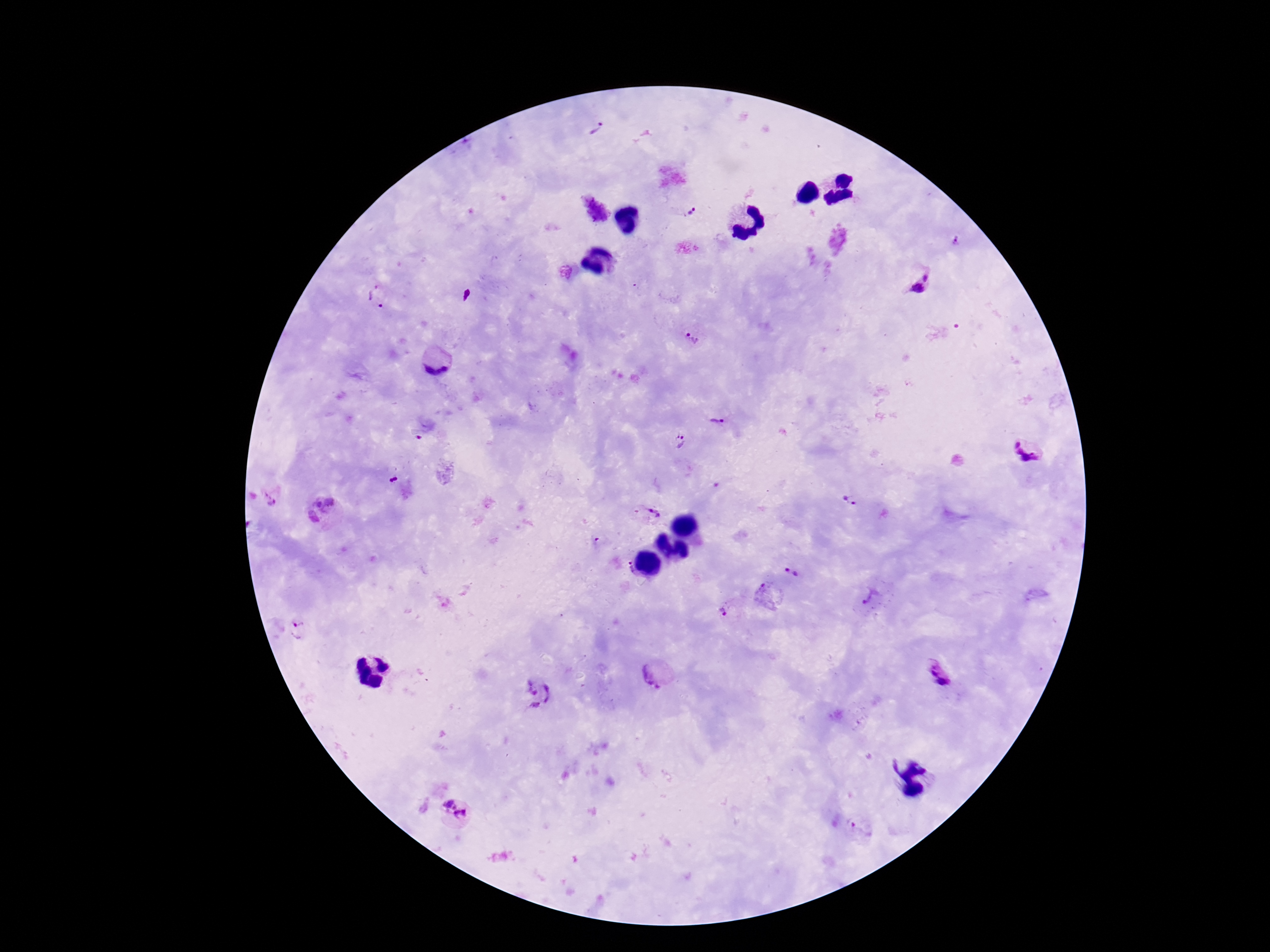

patient malaria status = positive
capture = smartphone camera through the microscope eyepiece
Plasmodium parasite locations = approximate centers as [x, y] in pixels: [597, 130], [693, 209], [957, 242], [925, 277], [917, 289], [376, 299], [692, 338], [435, 361], [716, 420], [418, 438], [679, 441], [1032, 449], [394, 480], [269, 499], [851, 500], [332, 502], [317, 503], [652, 513], [313, 518], [625, 570], [792, 571], [766, 594], [872, 599], [725, 612], [299, 630], [934, 671], [652, 674], [941, 682], [538, 694], [446, 801], [461, 817], [860, 829]
field of view = one from this slide
stain = Giemsa
image size = 1270×952 pixels
magnification = 100x
preparation = thick peripheral-blood smear